State the blood parasite species.
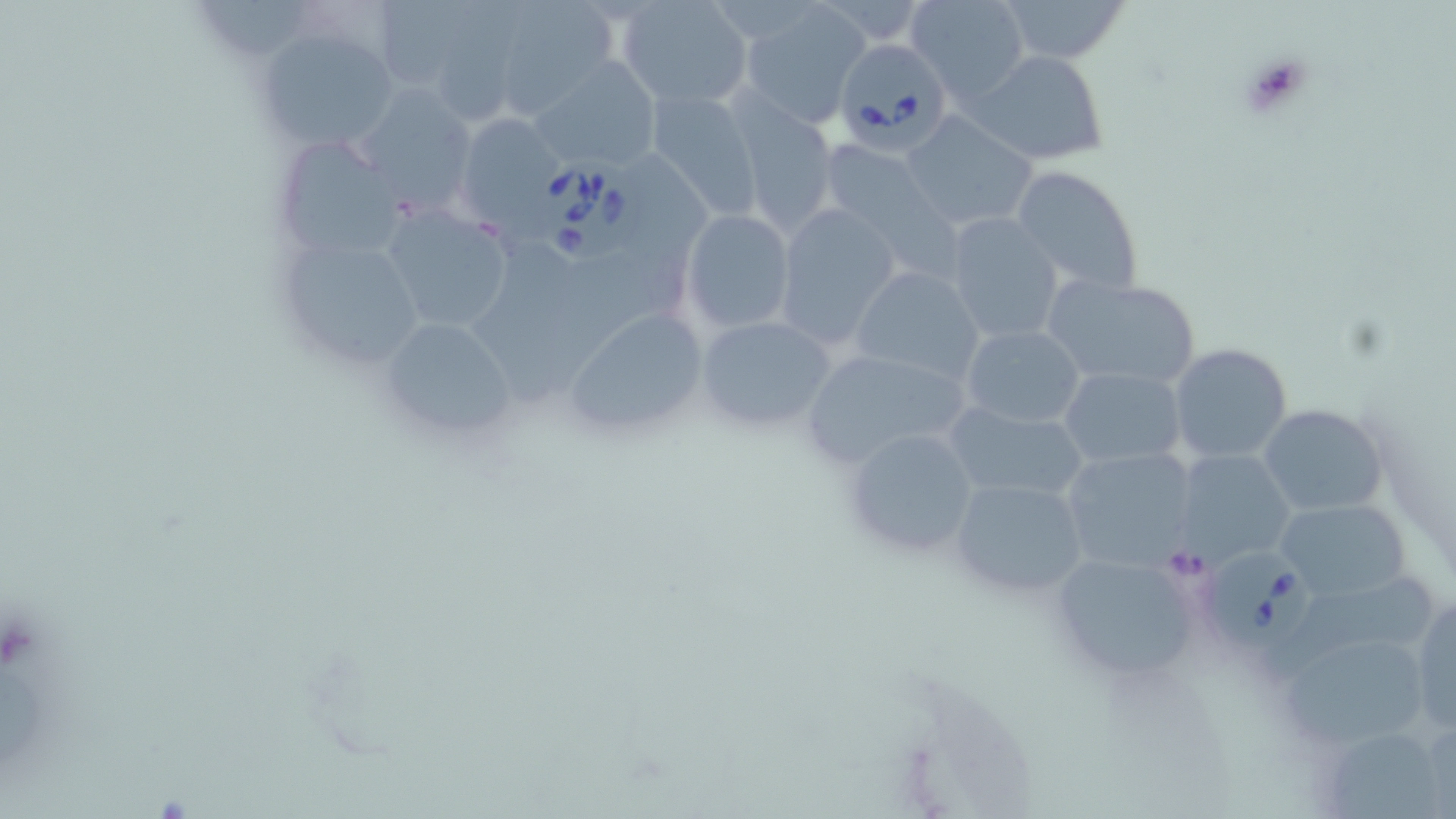
Babesia divergens.

Summary:
  - Coordinate format: approximate bounding boxes as (x1, y1, x2, y2) in pixels
  - Platelet locations: (1233, 49, 1319, 124)
  - Uninfected red blood cell locations: (507, 0, 615, 118), (615, 0, 751, 108), (906, 0, 1030, 101), (994, 0, 1132, 65), (736, 1, 870, 126), (370, 2, 466, 92), (430, 2, 541, 125), (256, 24, 402, 150), (971, 49, 1109, 164), (532, 57, 662, 172), (358, 72, 478, 216), (649, 91, 763, 220), (727, 100, 842, 233), (453, 112, 569, 233), (902, 114, 1037, 234), (272, 136, 404, 260), (816, 139, 948, 254), (1011, 164, 1144, 296), (771, 203, 902, 348), (379, 206, 512, 335), (682, 210, 794, 334), (943, 212, 1064, 344), (269, 230, 433, 369), (471, 230, 573, 410), (868, 237, 1042, 370), (547, 242, 674, 394), (850, 267, 986, 388), (1039, 271, 1202, 388), (565, 306, 709, 436), (693, 314, 839, 436), (376, 316, 520, 442), (960, 324, 1088, 429), (1167, 343, 1293, 464), (798, 346, 974, 470), (1059, 366, 1186, 468), (943, 401, 1090, 503), (1258, 403, 1389, 516), (839, 425, 980, 561), (1059, 446, 1201, 571), (1171, 450, 1296, 567), (948, 476, 1090, 600), (1274, 497, 1410, 602), (1045, 549, 1211, 688), (1260, 573, 1436, 680), (1411, 590, 1456, 731), (1286, 633, 1433, 749), (1335, 733, 1442, 819)
  - Babesia divergens-infected red blood cell locations: (833, 34, 957, 163), (528, 155, 651, 264), (1203, 550, 1312, 650)
  - Field of view: one of a larger specimen
  - Stain: May-Grünwald-Giemsa
  - Image size: 1456×819 pixels
  - Preparation: thin blood film
  - Modality: optical microscopy
  - Magnification: 1000x